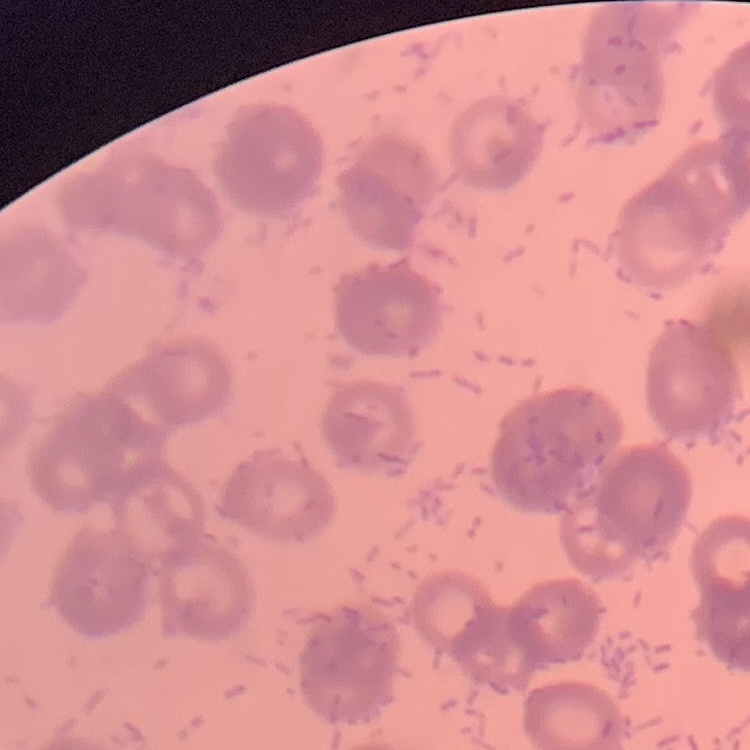

{
  "erythrocyte_morphology": "rouleaux formation",
  "stain": "Field's or Giemsa",
  "image_type": "one tile cut from a larger photomicrograph",
  "preparation": "thin blood smear"
}